State which parasite is depicted.
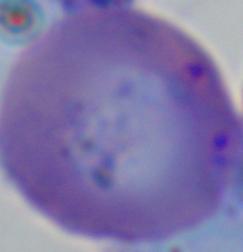

Babesia.

modality = micrograph
magnification = 1000x